Report the malaria status of this cell.
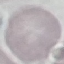

It is uninfected.

Automatically extracted cell patch, resized to 64 × 64 pixels. Giemsa-stained preparation. Acquired by smartphone through the microscope eyepiece. Thin blood film.